Report the malaria status of this cell.
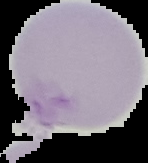
Uninfected.

{
  "preparation": "thin blood film",
  "image_size": "148×163 pixels",
  "image_type": "segmented cell region with the area outside set to black"
}